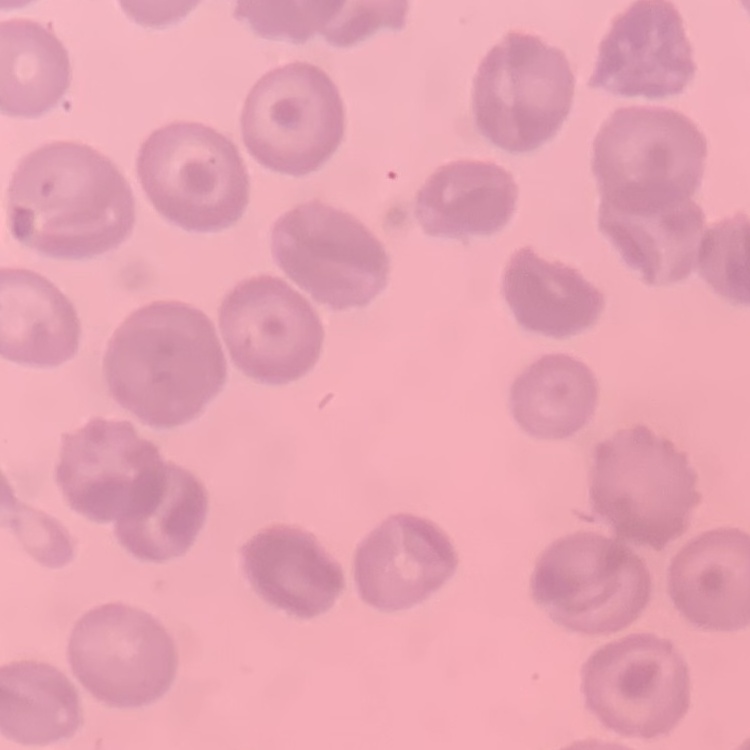

Summary:
  - Red blood cell morphology: no rouleaux formation
  - Stain: Field's or Giemsa
  - Preparation: thin blood smear
  - Image type: one tile cut from a larger photomicrograph